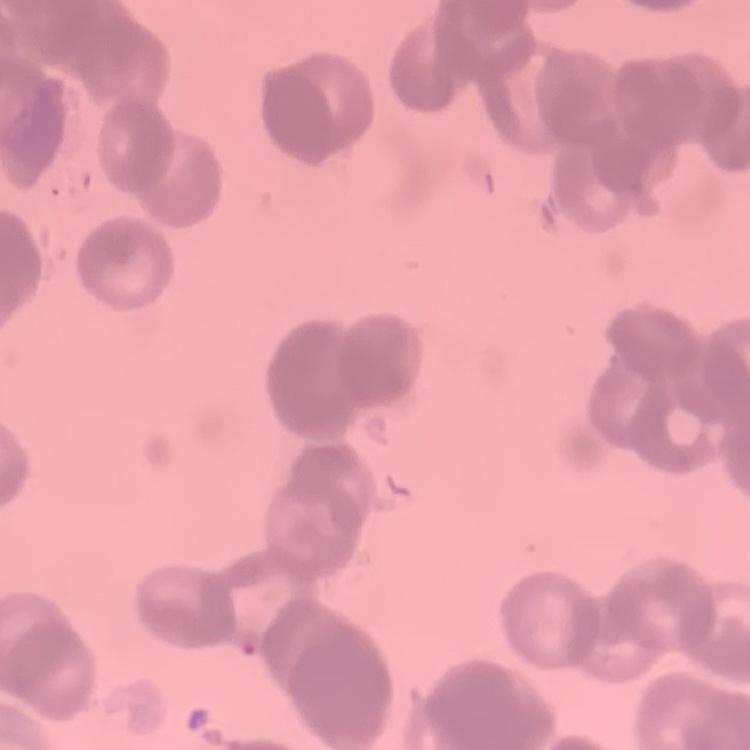
The erythrocytes show rouleaux formation. Thin peripheral smear. Stained with either Field's or Giemsa. Square crop of a larger photomicrograph.